Outline every parasitised red blood cell, every trophozoite, every gametocyte, every leukocyte, and every artifact (platelet-like body, stain precipitate, or debris).
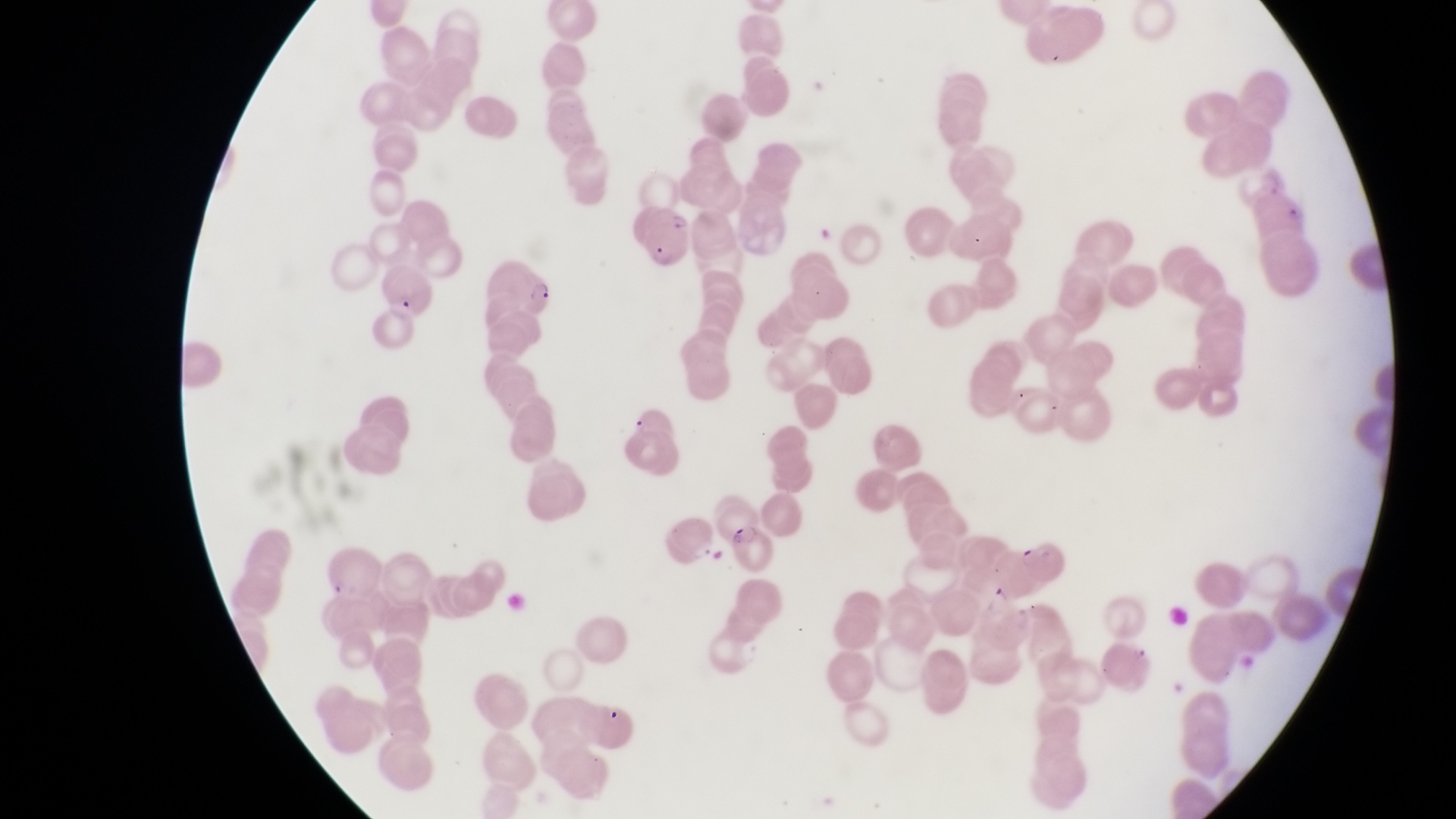
Approximate bounding boxes as left top right bottom in pixels.
Parasitised red blood cells: 641 201 696 268; 488 257 561 320; 373 290 429 354; 711 491 769 552; 1017 532 1073 584.
No leukocytes observed.

Summary:
  - Preparation: thin blood film
  - Magnification: 1000x
  - Field of view: single
  - Image size: 1456×819 pixels
  - Country: Uganda
  - Capture: smartphone photograph through the eyepiece of an Olympus CX-23 microscope